Locate every Plasmodium parasite.
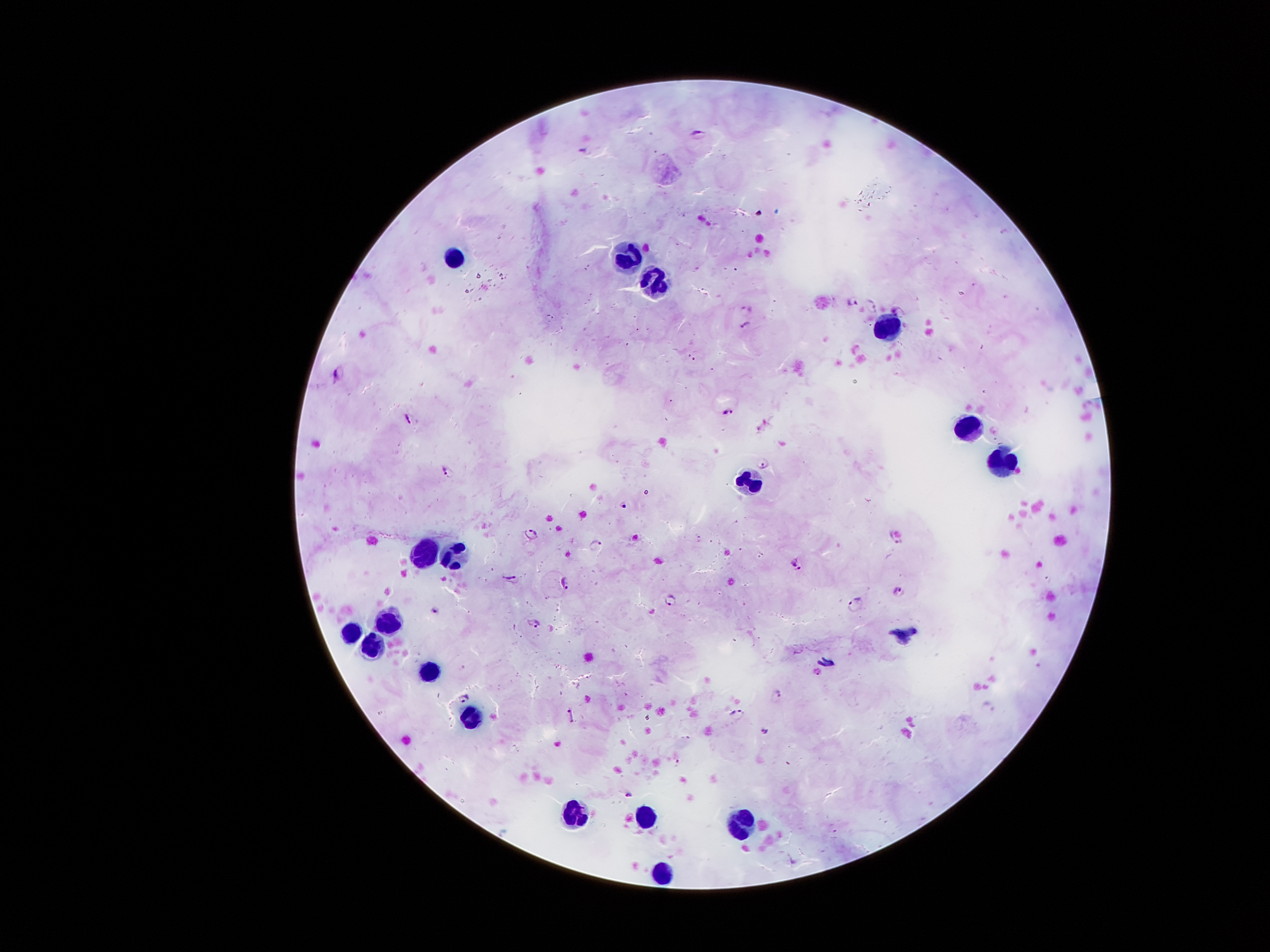
Approximate object centers, in pixels from the top-left corner.
Plasmodium parasites: (x=699, y=134), (x=583, y=151), (x=850, y=299), (x=869, y=302), (x=747, y=306), (x=898, y=310), (x=746, y=325), (x=338, y=372), (x=727, y=411), (x=410, y=419), (x=761, y=462), (x=448, y=473), (x=624, y=505), (x=531, y=535), (x=892, y=542), (x=594, y=544), (x=796, y=564), (x=511, y=578), (x=564, y=583), (x=900, y=590), (x=672, y=601), (x=856, y=603), (x=435, y=611), (x=533, y=622), (x=818, y=672), (x=775, y=694), (x=463, y=697), (x=738, y=714), (x=570, y=715), (x=765, y=731), (x=677, y=764), (x=629, y=795).

Leukocyte locations: (x=452, y=256), (x=628, y=258), (x=655, y=285), (x=888, y=328), (x=962, y=431), (x=1002, y=460), (x=749, y=482), (x=422, y=549), (x=448, y=551), (x=389, y=620), (x=347, y=631), (x=371, y=643), (x=427, y=670), (x=472, y=720), (x=572, y=810), (x=646, y=811), (x=737, y=820), (x=658, y=873). Thick blood film. Patient malaria status: infected with Plasmodium falciparum. Smartphone photograph taken through the microscope eyepiece. 100x magnification. Giemsa stain. Single field of view. Image is 1270×952 pixels.